State which parasite is depicted.
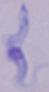

This is a trypanosome.

magnification = 1000x
modality = photomicrograph